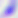
Summary:
  - Modality: photomicrograph
  - Identification: Toxoplasma gondii
  - Magnification: 400x